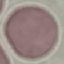
malaria status = uninfected
capture = smartphone through the microscope eyepiece
image type = cell patch, automatically extracted from a larger field of view and resized to 64 × 64 pixels
preparation = thin blood film
stain = Giemsa